Report the malaria status of this cell.
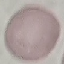
It is uninfected.

Thin blood smear. Photographed with a smartphone camera at the microscope eyepiece. Giemsa-stained preparation. Automatically extracted cell patch, resized to 64 × 64 pixels.